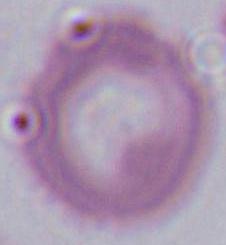

Summary:
  - Modality: micrograph
  - Magnification: 1000x
  - Identification: erythrocyte